Evaluate for parasitized red blood cells.
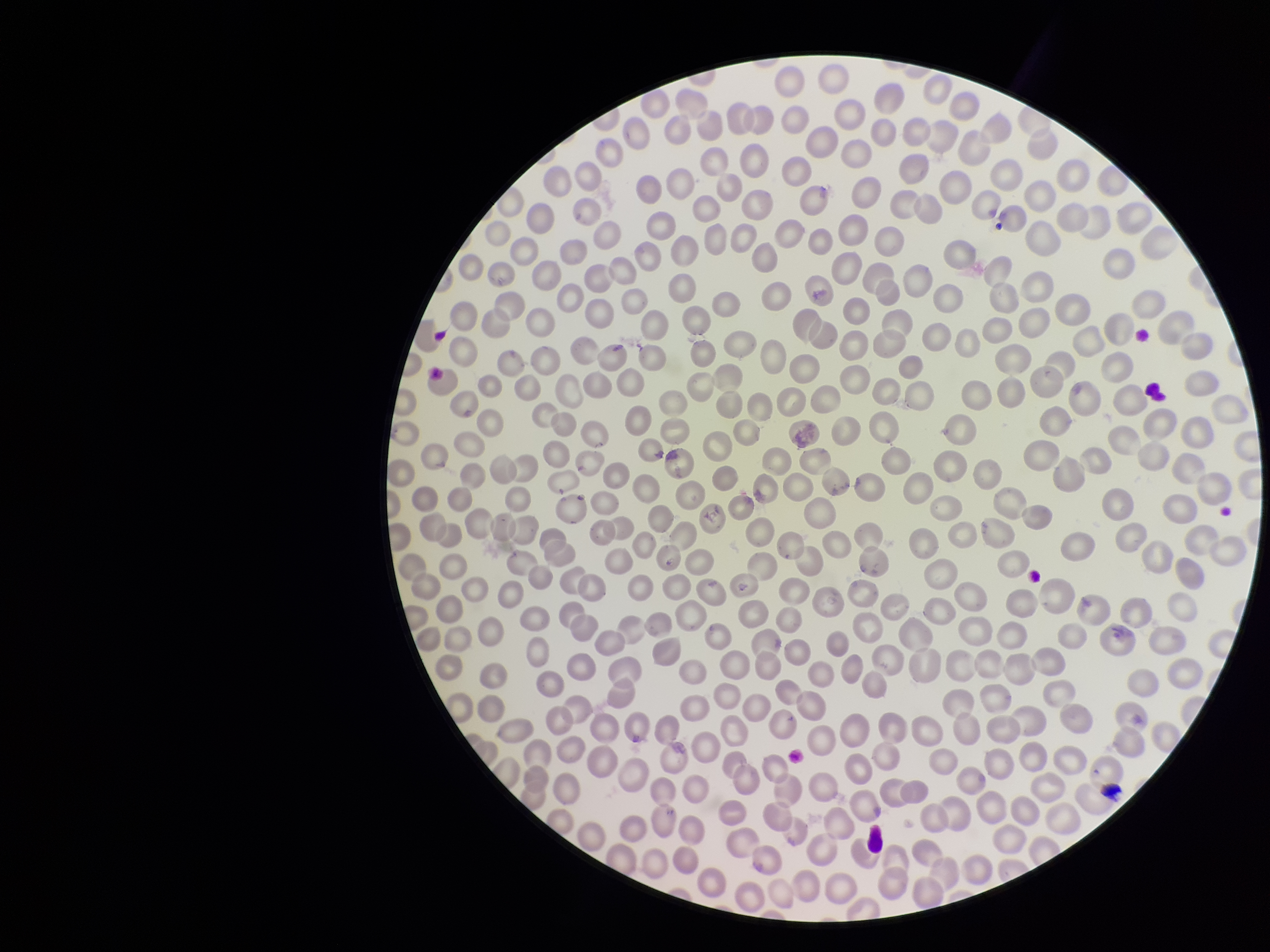
None identified.

field of view = single
capture = smartphone photograph through the microscope eyepiece
red blood cell count = 354
preparation = thin
parasitized red blood cell count = 0
species reported for this patient = Plasmodium falciparum
image size = 1270×952 pixels
patient malaria status = infected
stain = Giemsa